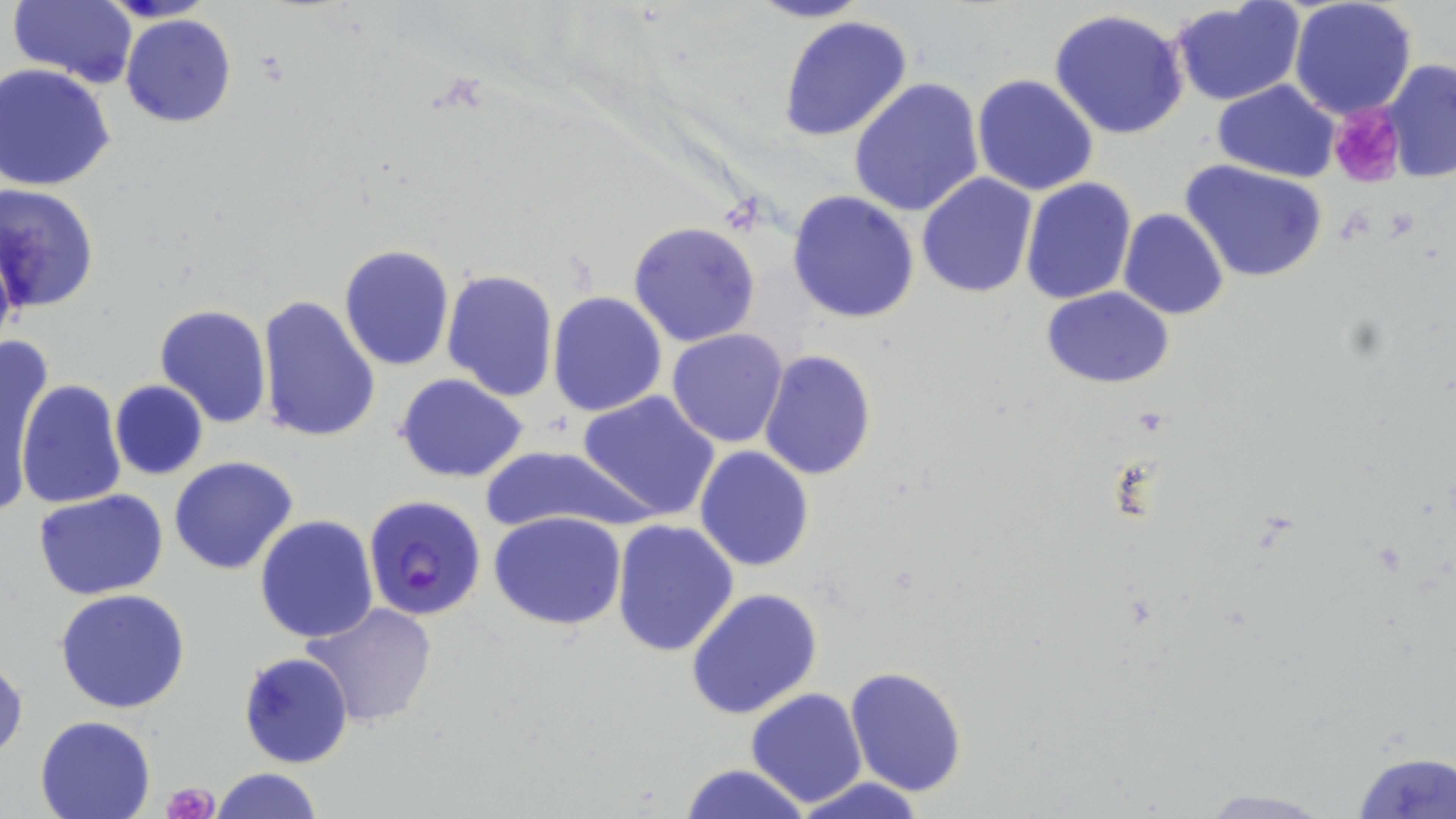
Summary:
  - Coordinate format: approximate bounding boxes as (x1, y1, x2, y2) in pixels
  - Platelet locations: (1332, 102, 1408, 188), (165, 781, 219, 818)
  - Uninfected red blood cell locations: (747, 0, 870, 24), (1289, 0, 1417, 119), (8, 2, 141, 86), (1170, 3, 1307, 108), (1047, 8, 1191, 140), (120, 13, 237, 128), (779, 14, 913, 142), (1381, 60, 1455, 184), (2, 63, 118, 192), (971, 73, 1099, 196), (847, 77, 986, 218), (1211, 79, 1340, 182), (1180, 159, 1329, 283), (915, 173, 1038, 299), (1020, 178, 1136, 305), (797, 184, 1041, 312), (1, 185, 101, 316), (787, 189, 920, 323), (1118, 208, 1229, 321), (626, 221, 761, 348), (338, 244, 453, 371), (442, 268, 558, 400), (1043, 286, 1174, 388), (549, 291, 668, 416), (255, 294, 381, 444), (153, 303, 272, 429), (665, 329, 789, 448), (1, 335, 46, 499), (758, 349, 878, 480), (393, 374, 530, 484), (16, 377, 125, 509), (110, 380, 208, 480), (3, 384, 31, 521), (576, 390, 720, 521), (480, 444, 642, 535), (695, 445, 815, 572), (169, 456, 298, 575), (34, 490, 168, 601), (488, 511, 627, 629), (255, 516, 378, 643), (611, 519, 740, 657), (685, 588, 824, 720), (57, 589, 191, 714), (301, 601, 441, 729), (237, 651, 354, 768), (1, 659, 27, 763), (844, 666, 967, 796), (745, 689, 869, 808), (34, 715, 158, 819), (1350, 751, 1455, 817), (678, 762, 812, 819), (211, 767, 324, 819), (786, 776, 932, 819), (1193, 788, 1339, 817)
  - Plasmodium falciparum-infected red blood cell locations: (363, 493, 489, 619)
  - Slide-level diagnosis: Plasmodium falciparum
  - Magnification: 1000x
  - Field of view: single
  - Modality: optical microscopy
  - Image size: 1456×819 pixels
  - Preparation: thin blood smear
  - Stain: May-Grünwald-Giemsa